Assess the background quality.
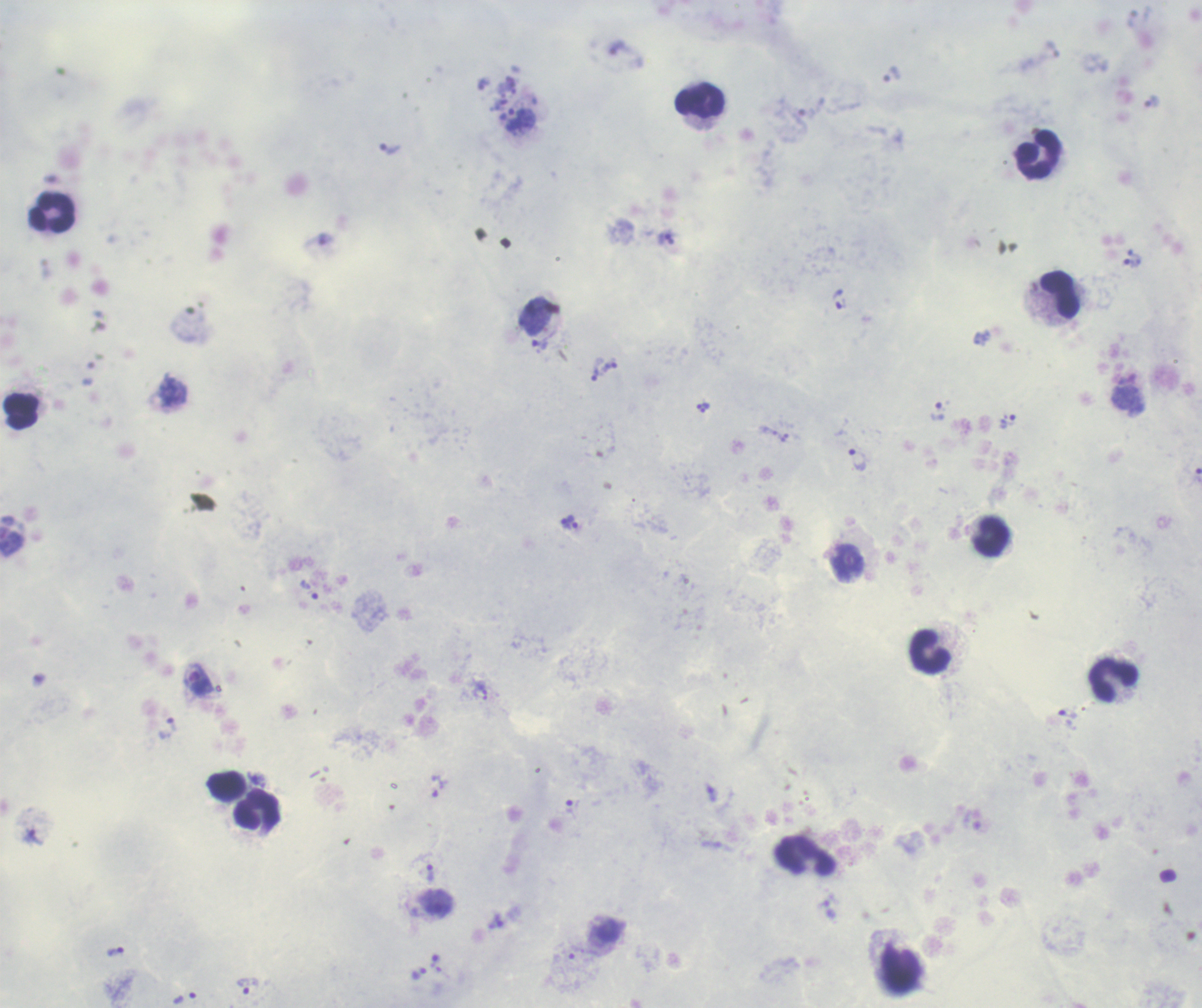

Satisfactory.

Approximate centers as {x, y} in pixels. Leukocyte locations: {700, 100}, {1038, 154}, {53, 213}, {1060, 295}, {21, 411}, {992, 536}, {931, 652}, {1113, 680}, {258, 809}, {805, 855}. Trophozoite locations: {520, 118}, {390, 150}, {665, 238}, {1132, 262}, {540, 344}, {598, 375}, {937, 410}, {1009, 422}, {857, 459}, {565, 520}, {573, 525}, {309, 590}, {198, 680}, {1067, 712}, {168, 729}, {437, 785}, {711, 794}, {573, 807}, {430, 873}, {498, 921}, {116, 952}, {419, 973}, {248, 986}, {186, 998}. Image is 1202×1008 pixels. Romanowsky-stained preparation. Captured at 100x magnification. Thick smear of blood. Previously used in a real diagnosis. Coloration quality: good. Result: positive for malaria parasites. One field from this slide.